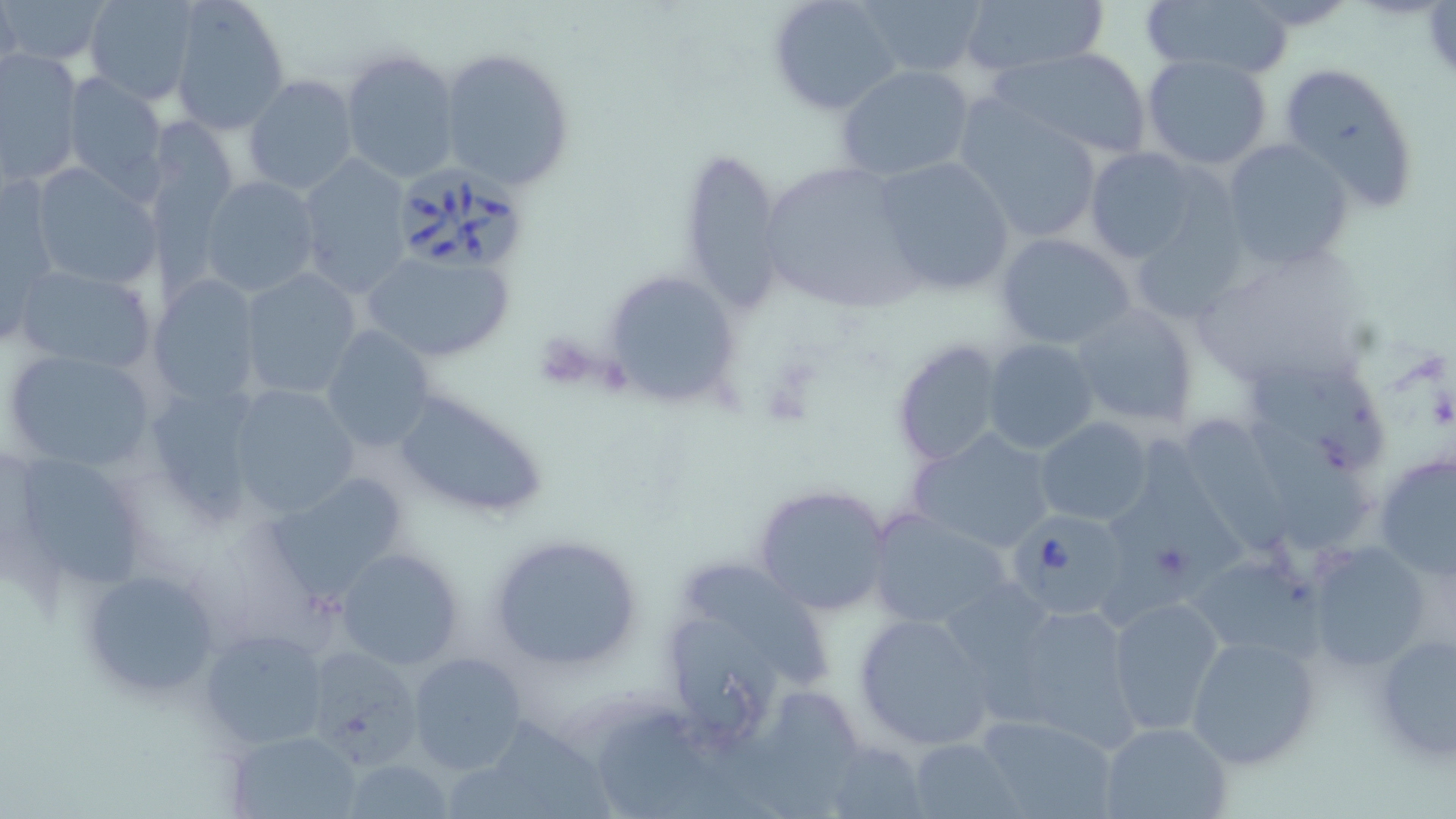

slide-level diagnosis = Babesia divergens
stain = May-Grünwald-Giemsa
Babesia divergens-infected red blood cell locations = approximate bounding boxes as named x1/y1/x2/y2 corners in pixels: (x1=400, y1=163, x2=528, y2=272), (x1=1005, y1=510, x2=1132, y2=620)
image size = 1456×819 pixels
magnification = 1000x
preparation = thin blood smear
field of view = one of a larger specimen
platelet locations = approximate bounding boxes as named x1/y1/x2/y2 corners in pixels: (x1=531, y1=332, x2=600, y2=392), (x1=761, y1=359, x2=822, y2=419)
uninfected red blood cell locations = approximate bounding boxes as named x1/y1/x2/y2 corners in pixels: (x1=1, y1=0, x2=108, y2=64), (x1=1, y1=0, x2=22, y2=93), (x1=83, y1=0, x2=200, y2=104), (x1=170, y1=0, x2=289, y2=134), (x1=771, y1=0, x2=903, y2=114), (x1=858, y1=0, x2=989, y2=78), (x1=1142, y1=0, x2=1291, y2=80), (x1=958, y1=1, x2=1110, y2=79), (x1=339, y1=46, x2=460, y2=185), (x1=993, y1=46, x2=1151, y2=161), (x1=437, y1=48, x2=575, y2=192), (x1=0, y1=49, x2=83, y2=185), (x1=1141, y1=53, x2=1276, y2=169), (x1=1278, y1=61, x2=1423, y2=212), (x1=835, y1=65, x2=978, y2=182), (x1=61, y1=72, x2=168, y2=196), (x1=243, y1=75, x2=360, y2=193), (x1=953, y1=98, x2=1106, y2=244), (x1=136, y1=113, x2=242, y2=310), (x1=1222, y1=138, x2=1355, y2=270), (x1=680, y1=146, x2=786, y2=309), (x1=1085, y1=147, x2=1204, y2=264), (x1=296, y1=152, x2=413, y2=298), (x1=873, y1=156, x2=1017, y2=294), (x1=758, y1=159, x2=927, y2=318), (x1=28, y1=163, x2=162, y2=292), (x1=199, y1=175, x2=321, y2=298), (x1=2, y1=177, x2=58, y2=336), (x1=1127, y1=198, x2=1253, y2=328), (x1=994, y1=231, x2=1138, y2=350), (x1=1194, y1=243, x2=1375, y2=394), (x1=358, y1=247, x2=518, y2=365), (x1=12, y1=263, x2=159, y2=376), (x1=603, y1=268, x2=740, y2=409), (x1=238, y1=269, x2=363, y2=398), (x1=151, y1=276, x2=260, y2=407), (x1=1069, y1=304, x2=1201, y2=429), (x1=320, y1=325, x2=436, y2=453), (x1=891, y1=338, x2=1005, y2=469), (x1=984, y1=339, x2=1100, y2=455), (x1=3, y1=347, x2=160, y2=474), (x1=1252, y1=365, x2=1384, y2=477), (x1=227, y1=383, x2=360, y2=517), (x1=143, y1=384, x2=267, y2=524), (x1=390, y1=389, x2=550, y2=521), (x1=1181, y1=412, x2=1290, y2=554), (x1=1036, y1=417, x2=1153, y2=525), (x1=1250, y1=418, x2=1366, y2=551), (x1=908, y1=427, x2=1058, y2=554), (x1=1096, y1=434, x2=1238, y2=628), (x1=5, y1=450, x2=155, y2=597), (x1=1373, y1=451, x2=1456, y2=577), (x1=273, y1=474, x2=410, y2=605), (x1=753, y1=484, x2=894, y2=616), (x1=866, y1=509, x2=1014, y2=632), (x1=486, y1=534, x2=645, y2=674), (x1=1307, y1=540, x2=1434, y2=672), (x1=334, y1=548, x2=464, y2=669), (x1=1184, y1=558, x2=1322, y2=663), (x1=687, y1=564, x2=830, y2=693), (x1=78, y1=565, x2=223, y2=698), (x1=1105, y1=594, x2=1227, y2=734), (x1=992, y1=597, x2=1142, y2=750), (x1=852, y1=611, x2=997, y2=749), (x1=673, y1=618, x2=786, y2=738), (x1=202, y1=630, x2=330, y2=748), (x1=1368, y1=630, x2=1456, y2=766), (x1=1186, y1=633, x2=1322, y2=770), (x1=303, y1=641, x2=430, y2=765), (x1=407, y1=652, x2=525, y2=774), (x1=715, y1=691, x2=869, y2=819), (x1=602, y1=711, x2=772, y2=819), (x1=973, y1=714, x2=1120, y2=819), (x1=1098, y1=720, x2=1233, y2=819), (x1=497, y1=721, x2=611, y2=819), (x1=229, y1=730, x2=362, y2=818), (x1=909, y1=736, x2=1018, y2=817), (x1=814, y1=739, x2=929, y2=818), (x1=341, y1=759, x2=455, y2=818), (x1=448, y1=766, x2=563, y2=819)
modality = optical microscopy